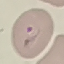
malaria status = parasitized
image type = automatically extracted cell patch, resized to 64 × 64 pixels
stain = Giemsa
preparation = thin blood film
capture = smartphone through the microscope eyepiece